Give the extent of all Plasmodium falciparum-infected red blood cells.
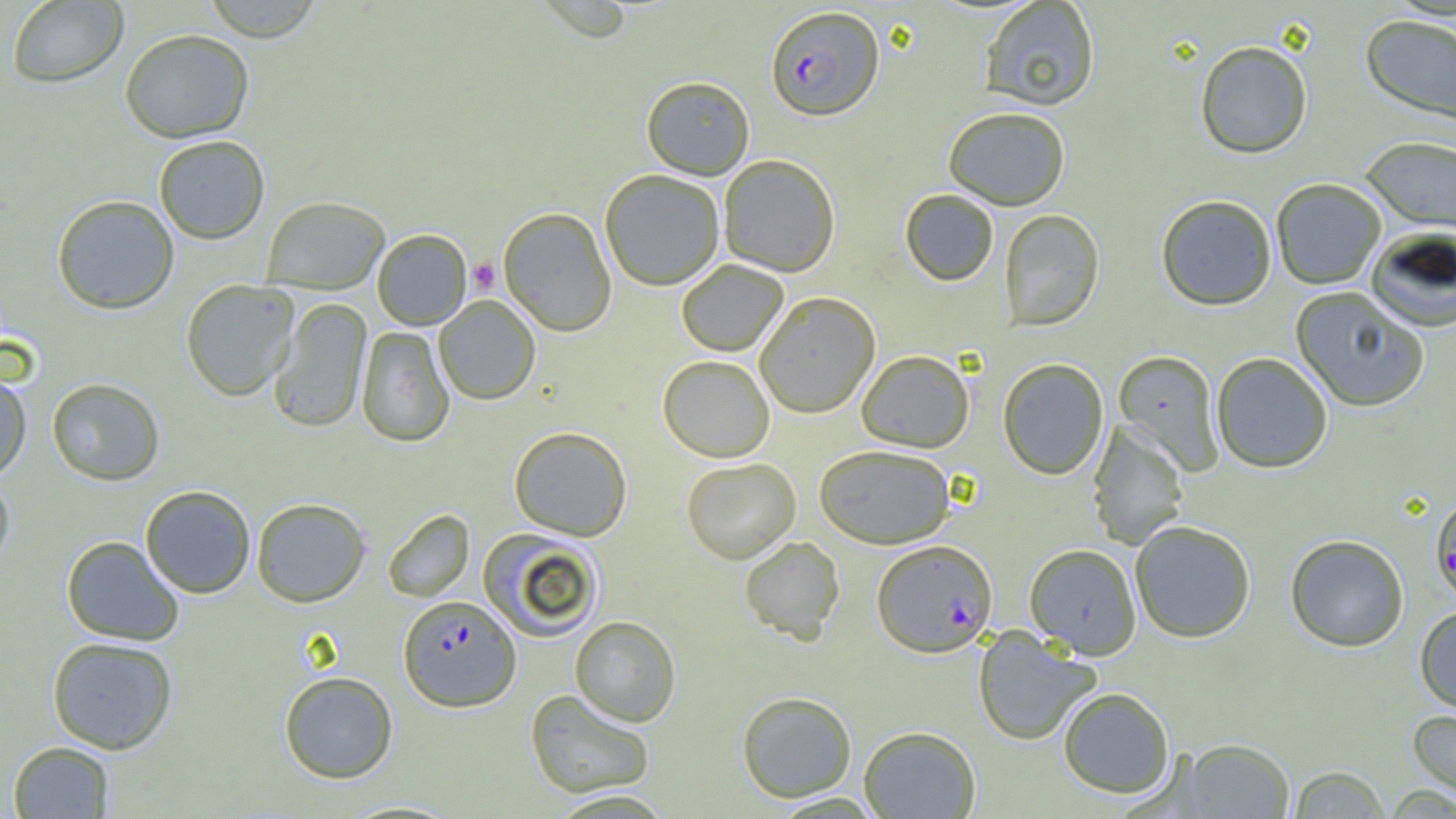

Approximate bounding boxes as named x1/y1/x2/y2 corners in pixels.
Plasmodium falciparum-infected red blood cells: (x1=765, y1=5, x2=884, y2=121), (x1=1429, y1=494, x2=1456, y2=603), (x1=872, y1=540, x2=998, y2=657), (x1=398, y1=595, x2=520, y2=711).

Summary:
  - Uninfected red blood cell locations: (x1=6, y1=1, x2=128, y2=89), (x1=200, y1=1, x2=326, y2=42), (x1=979, y1=1, x2=1100, y2=112), (x1=1359, y1=15, x2=1456, y2=129), (x1=119, y1=29, x2=255, y2=143), (x1=1194, y1=41, x2=1313, y2=160), (x1=641, y1=76, x2=755, y2=179), (x1=943, y1=107, x2=1071, y2=211), (x1=153, y1=135, x2=270, y2=244), (x1=1359, y1=136, x2=1456, y2=233), (x1=718, y1=154, x2=840, y2=276), (x1=599, y1=170, x2=725, y2=290), (x1=1271, y1=179, x2=1387, y2=290), (x1=900, y1=190, x2=999, y2=286), (x1=51, y1=194, x2=180, y2=314), (x1=1156, y1=195, x2=1277, y2=312), (x1=260, y1=196, x2=391, y2=293), (x1=498, y1=207, x2=616, y2=336), (x1=998, y1=209, x2=1104, y2=332), (x1=1366, y1=228, x2=1456, y2=333), (x1=372, y1=229, x2=472, y2=330), (x1=676, y1=260, x2=789, y2=357), (x1=180, y1=279, x2=299, y2=402), (x1=1290, y1=287, x2=1430, y2=413), (x1=755, y1=292, x2=880, y2=418), (x1=433, y1=295, x2=541, y2=405), (x1=268, y1=298, x2=371, y2=433), (x1=356, y1=326, x2=455, y2=447), (x1=856, y1=350, x2=974, y2=452), (x1=1113, y1=350, x2=1225, y2=476), (x1=1211, y1=353, x2=1332, y2=474), (x1=658, y1=355, x2=774, y2=462), (x1=997, y1=358, x2=1108, y2=480), (x1=0, y1=370, x2=32, y2=482), (x1=46, y1=377, x2=166, y2=486), (x1=1087, y1=422, x2=1190, y2=550), (x1=508, y1=426, x2=632, y2=540), (x1=814, y1=445, x2=955, y2=548), (x1=681, y1=458, x2=801, y2=564), (x1=0, y1=474, x2=16, y2=573), (x1=140, y1=484, x2=256, y2=598), (x1=251, y1=497, x2=371, y2=607), (x1=382, y1=509, x2=475, y2=602), (x1=1129, y1=520, x2=1256, y2=644), (x1=478, y1=528, x2=605, y2=642), (x1=1284, y1=534, x2=1409, y2=653), (x1=61, y1=535, x2=185, y2=646), (x1=739, y1=536, x2=845, y2=645), (x1=1025, y1=544, x2=1142, y2=659), (x1=1414, y1=606, x2=1456, y2=714), (x1=570, y1=616, x2=681, y2=726), (x1=972, y1=628, x2=1101, y2=746), (x1=46, y1=636, x2=178, y2=754), (x1=278, y1=671, x2=398, y2=783), (x1=1058, y1=687, x2=1175, y2=799), (x1=525, y1=688, x2=655, y2=798), (x1=736, y1=691, x2=857, y2=802), (x1=1406, y1=708, x2=1456, y2=803), (x1=859, y1=726, x2=981, y2=819), (x1=1178, y1=738, x2=1295, y2=818), (x1=7, y1=741, x2=114, y2=818), (x1=1287, y1=765, x2=1391, y2=818), (x1=546, y1=789, x2=676, y2=818)
  - Platelet locations: (x1=468, y1=258, x2=500, y2=294)
  - Slide-level diagnosis: Plasmodium falciparum
  - Magnification: 1000x
  - Modality: light microscopy
  - Preparation: thin blood smear
  - Image size: 1456×819 pixels
  - Field of view: one of a larger specimen